Locate every Plasmodium parasite and every leukocyte.
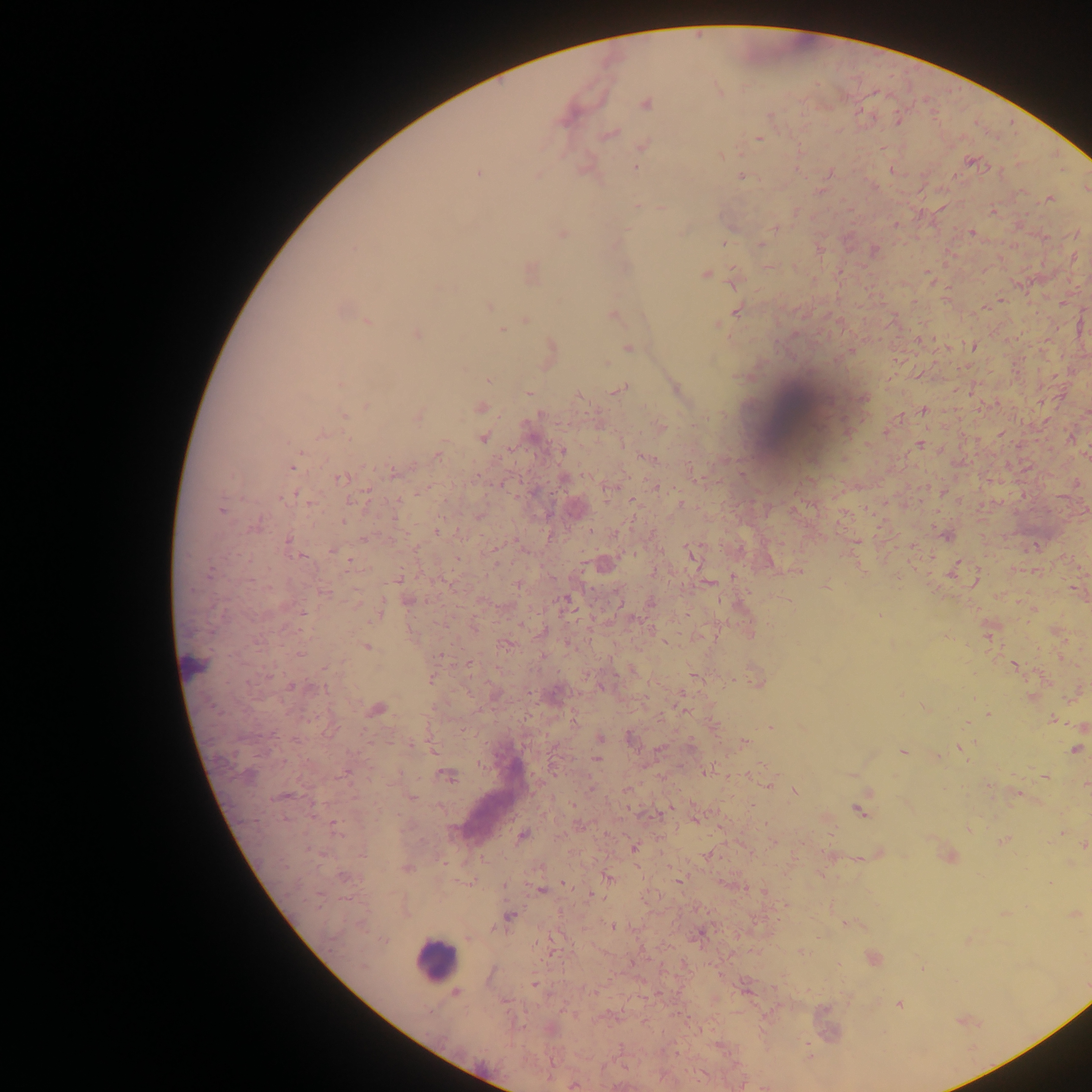
Approximate centers as {x, y} in pixels.
Plasmodium parasites: {646, 104}, {770, 116}, {610, 134}, {758, 138}, {643, 146}, {970, 160}, {636, 167}, {892, 170}, {478, 173}, {537, 175}, {741, 177}, {1087, 189}, {1049, 198}, {636, 206}, {661, 208}, {992, 212}, {776, 228}, {971, 232}, {562, 234}, {724, 242}, {761, 245}, {874, 249}, {769, 267}, {530, 272}, {705, 274}, {733, 279}, {490, 306}, {736, 311}, {613, 315}, {525, 319}, {368, 321}, {718, 325}, {501, 330}, {416, 334}, {628, 347}, {973, 347}, {551, 348}, {606, 363}, {488, 380}, {341, 384}, {622, 389}, {676, 391}, {528, 393}, {580, 396}, {864, 398}, {366, 406}, {480, 407}, {922, 410}, {342, 415}, {418, 415}, {660, 428}, {888, 431}, {322, 435}, {484, 438}, {920, 444}, {562, 451}, {438, 456}, {646, 457}, {293, 467}, {394, 473}, {340, 479}, {655, 486}, {284, 497}, {353, 501}, {680, 504}, {221, 511}, {257, 525}, {437, 531}, {945, 535}, {364, 538}, {289, 542}, {691, 554}, {300, 557}, {349, 561}, {769, 563}, {603, 565}, {952, 571}, {209, 573}, {398, 579}, {976, 581}, {710, 583}, {825, 587}, {566, 600}, {408, 601}, {651, 603}, {303, 613}, {379, 613}, {881, 615}, {988, 634}, {257, 642}, {664, 642}, {505, 644}, {366, 647}, {301, 654}, {440, 654}, {1013, 665}, {268, 675}, {756, 679}, {431, 680}, {291, 686}, {602, 687}, {1031, 696}, {925, 708}, {377, 710}, {683, 710}, {987, 714}, {1053, 720}, {770, 726}, {599, 737}, {631, 739}, {745, 743}, {411, 746}, {434, 749}, {659, 749}, {962, 749}, {1074, 749}, {902, 752}, {596, 759}, {707, 771}, {345, 773}, {446, 774}, {249, 775}, {1045, 777}, {767, 784}, {1086, 785}, {796, 792}, {1017, 794}, {284, 796}, {412, 797}, {859, 810}, {695, 819}, {336, 828}, {522, 836}, {1003, 841}, {1084, 845}, {634, 848}, {362, 854}, {708, 857}, {407, 868}, {343, 877}, {608, 878}, {678, 880}, {565, 884}, {540, 890}, {591, 895}, {1075, 914}, {509, 916}, {847, 924}, {613, 926}, {699, 933}, {384, 940}, {802, 951}, {874, 958}, {534, 984}, {456, 992}, {899, 1004}, {574, 1086}.
Leukocytes: {800, 411}, {190, 666}, {436, 960}.

Sample from Ghana. Thick blood smear. Photographed through a microscope with a mobile-phone camera. Single field of view. Image is 1092×1092 pixels.